Outline each blood parasite and name the species.
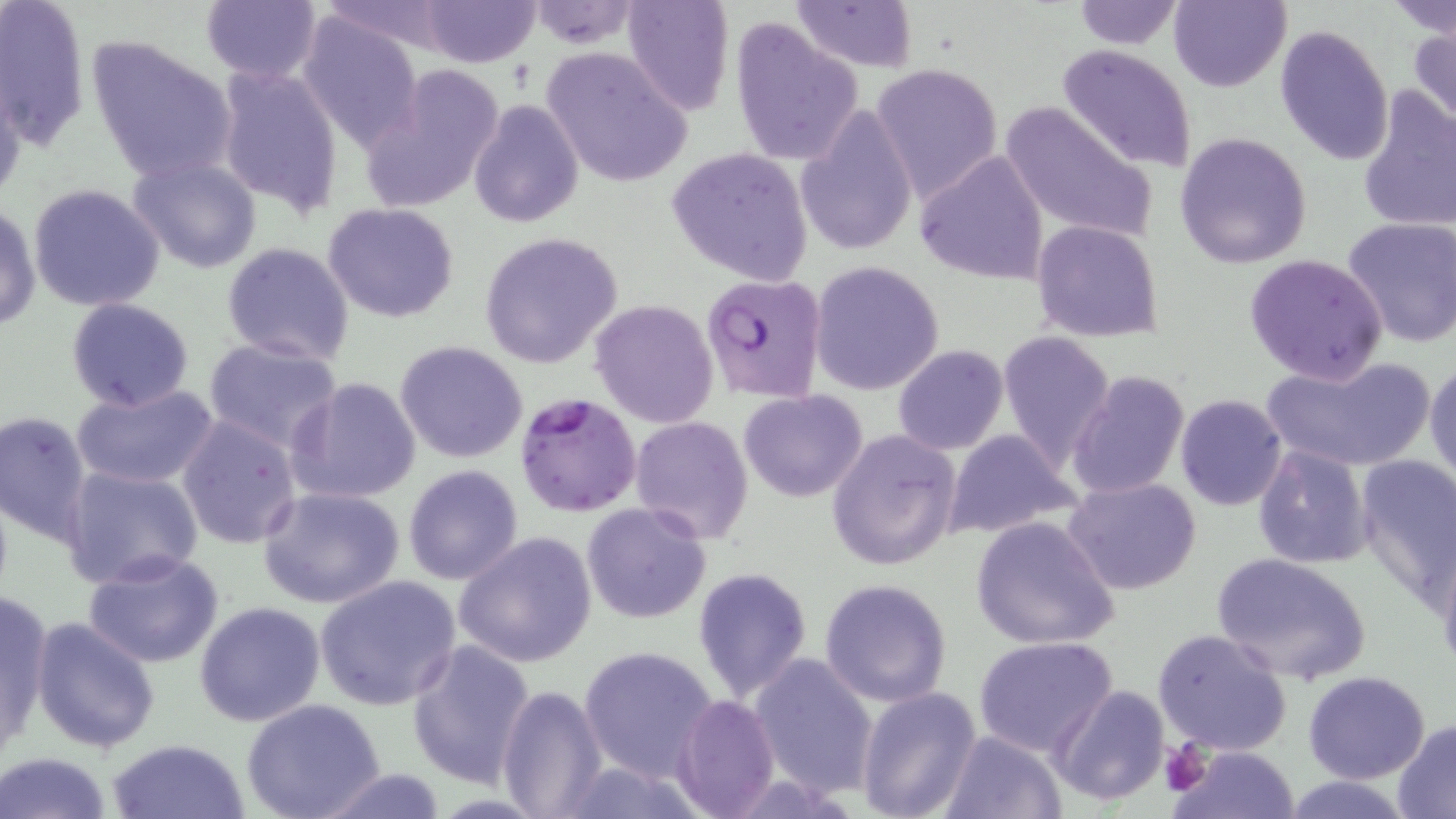

Approximate bounding boxes as named x1/y1/x2/y2 corners in pixels.
Plasmodium falciparum-infected red blood cells: (x1=700, y1=273, x2=826, y2=403), (x1=514, y1=391, x2=641, y2=518).
No Plasmodium ovale, Plasmodium malariae, Plasmodium vivax, Babesia divergens, or Trypanosoma brucei observed.

Uninfected red blood cell locations: (x1=200, y1=0, x2=324, y2=84), (x1=790, y1=0, x2=916, y2=72), (x1=1169, y1=0, x2=1291, y2=92), (x1=1, y1=1, x2=90, y2=149), (x1=416, y1=1, x2=542, y2=66), (x1=524, y1=1, x2=642, y2=48), (x1=621, y1=1, x2=734, y2=115), (x1=1071, y1=1, x2=1184, y2=48), (x1=1388, y1=1, x2=1456, y2=40), (x1=294, y1=14, x2=424, y2=151), (x1=727, y1=20, x2=864, y2=165), (x1=1408, y1=25, x2=1456, y2=128), (x1=1274, y1=26, x2=1394, y2=165), (x1=87, y1=34, x2=238, y2=182), (x1=1058, y1=44, x2=1200, y2=173), (x1=542, y1=48, x2=694, y2=188), (x1=871, y1=62, x2=1003, y2=201), (x1=360, y1=64, x2=507, y2=216), (x1=216, y1=65, x2=344, y2=214), (x1=0, y1=71, x2=28, y2=204), (x1=1356, y1=85, x2=1456, y2=234), (x1=468, y1=98, x2=583, y2=228), (x1=999, y1=100, x2=1158, y2=248), (x1=796, y1=103, x2=919, y2=258), (x1=1175, y1=132, x2=1312, y2=269), (x1=666, y1=146, x2=813, y2=287), (x1=916, y1=148, x2=1048, y2=286), (x1=127, y1=156, x2=262, y2=274), (x1=26, y1=184, x2=166, y2=314), (x1=322, y1=201, x2=460, y2=322), (x1=0, y1=202, x2=41, y2=334), (x1=1343, y1=217, x2=1456, y2=348), (x1=1032, y1=220, x2=1164, y2=340), (x1=478, y1=231, x2=624, y2=370), (x1=221, y1=243, x2=355, y2=367), (x1=1243, y1=253, x2=1390, y2=385), (x1=809, y1=261, x2=946, y2=397), (x1=66, y1=297, x2=195, y2=413), (x1=591, y1=298, x2=718, y2=429), (x1=998, y1=331, x2=1117, y2=469), (x1=203, y1=337, x2=343, y2=453), (x1=394, y1=340, x2=528, y2=462), (x1=893, y1=344, x2=1008, y2=455), (x1=1263, y1=353, x2=1437, y2=473), (x1=1426, y1=360, x2=1456, y2=489), (x1=1066, y1=369, x2=1189, y2=501), (x1=287, y1=377, x2=422, y2=503), (x1=71, y1=381, x2=219, y2=492), (x1=739, y1=390, x2=868, y2=502), (x1=1175, y1=395, x2=1288, y2=510), (x1=1, y1=410, x2=93, y2=546), (x1=178, y1=413, x2=303, y2=550), (x1=630, y1=414, x2=754, y2=543), (x1=826, y1=429, x2=960, y2=570), (x1=941, y1=429, x2=1080, y2=542), (x1=1252, y1=443, x2=1372, y2=570), (x1=1354, y1=455, x2=1456, y2=604), (x1=402, y1=465, x2=523, y2=585), (x1=60, y1=466, x2=204, y2=590), (x1=1064, y1=477, x2=1203, y2=596), (x1=259, y1=486, x2=406, y2=610), (x1=581, y1=503, x2=710, y2=624), (x1=970, y1=515, x2=1120, y2=651), (x1=452, y1=531, x2=597, y2=669), (x1=82, y1=550, x2=225, y2=668), (x1=1209, y1=553, x2=1372, y2=685), (x1=692, y1=567, x2=812, y2=702), (x1=314, y1=576, x2=460, y2=709), (x1=818, y1=577, x2=952, y2=706), (x1=0, y1=589, x2=53, y2=758), (x1=194, y1=600, x2=327, y2=727), (x1=31, y1=616, x2=161, y2=754), (x1=1153, y1=628, x2=1292, y2=755), (x1=973, y1=636, x2=1118, y2=757), (x1=405, y1=638, x2=536, y2=788), (x1=578, y1=647, x2=716, y2=779), (x1=747, y1=652, x2=879, y2=799), (x1=1304, y1=671, x2=1432, y2=784), (x1=496, y1=683, x2=607, y2=819), (x1=1050, y1=683, x2=1172, y2=806), (x1=856, y1=684, x2=982, y2=819), (x1=672, y1=694, x2=780, y2=817), (x1=241, y1=700, x2=387, y2=819), (x1=1392, y1=719, x2=1456, y2=814), (x1=939, y1=729, x2=1065, y2=818), (x1=104, y1=738, x2=252, y2=819), (x1=1169, y1=743, x2=1300, y2=819), (x1=1, y1=752, x2=115, y2=819), (x1=310, y1=765, x2=451, y2=819), (x1=1278, y1=775, x2=1417, y2=818). Platelet locations: (x1=1160, y1=743, x2=1212, y2=795). Slide-level diagnosis: Plasmodium falciparum. Image is 1456×819 pixels. Single field of view. Optical microscopy. Captured at 1000x magnification. Thin blood smear. May-Grünwald-Giemsa stain.